Assess this cell for malaria.
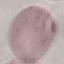

It is uninfected.

Acquired by smartphone through the microscope eyepiece. Giemsa-stained preparation. Automatically extracted cell patch, resized to 64 × 64 pixels. Thin blood smear.